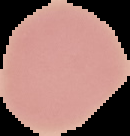

{
  "image_type": "cell region segmented out of the field of view; surrounding area masked to black",
  "image_size": "130×136 pixels",
  "preparation": "thin blood smear",
  "malaria_status": "uninfected"
}